Assess this cell for malaria.
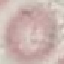

Uninfected.

Acquired by smartphone through the microscope eyepiece. Thin blood smear. Giemsa stain. Cell patch, automatically extracted from a larger field of view and resized to 64 × 64 pixels.